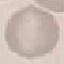

Summary:
  - Malaria status: uninfected
  - Stain: Giemsa
  - Preparation: thin smear
  - Image type: automatically extracted cell patch, resized to 64 × 64 pixels
  - Capture: smartphone camera at the microscope eyepiece